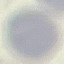
result = no malaria parasites seen
preparation = thin blood smear
image type = cell patch, automatically extracted from a larger field of view and resized to 64 × 64 pixels
capture = smartphone through the microscope eyepiece
stain = Giemsa